Locate and identify every blood parasite.
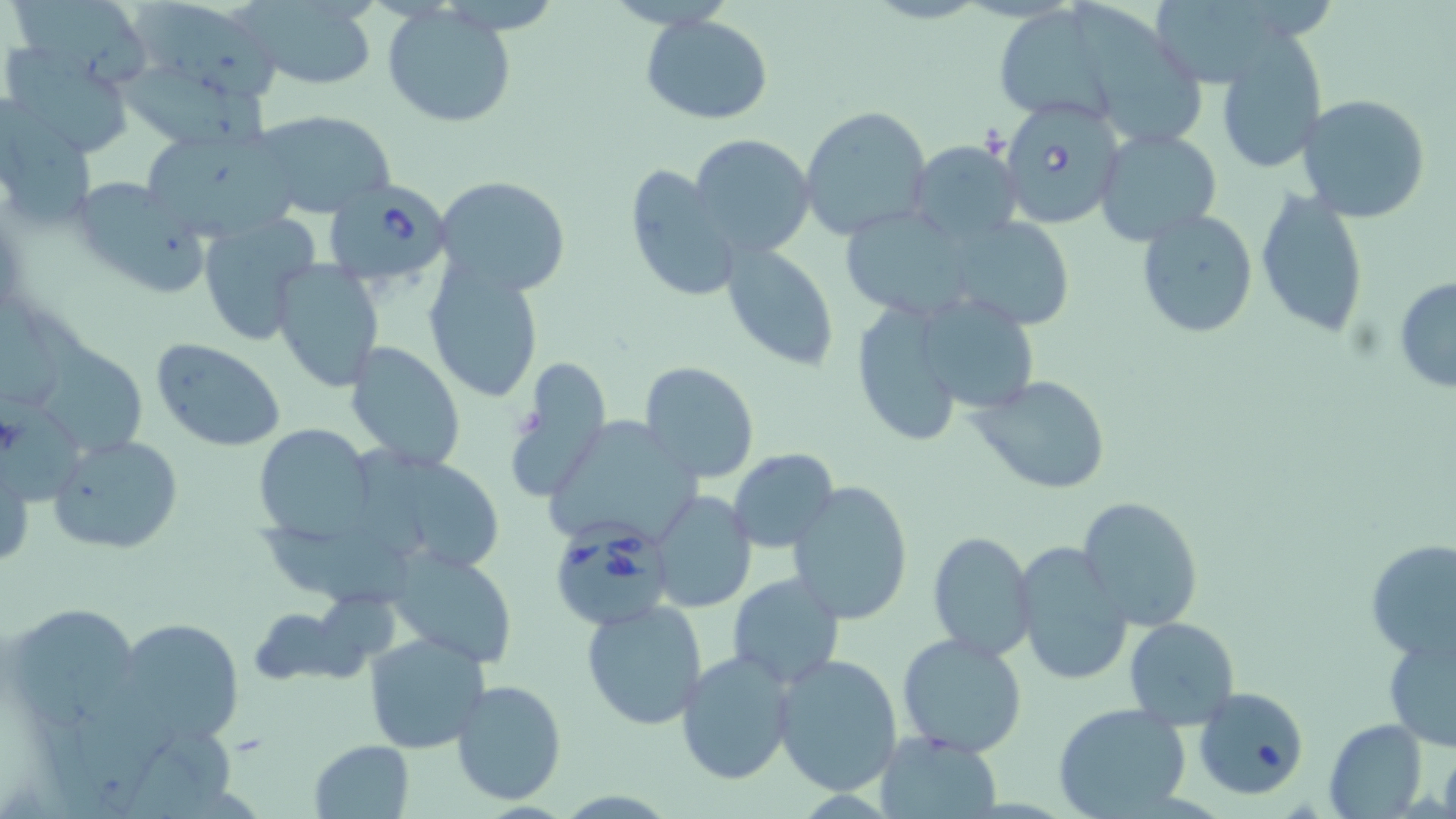
Approximate bounding boxes as [x1, y1, x2, y2] in pixels.
Babesia divergens-infected red blood cells: [995, 98, 1126, 229], [326, 177, 455, 289], [549, 515, 677, 630], [1193, 686, 1310, 801].
No Plasmodium falciparum, Plasmodium ovale, Plasmodium malariae, Plasmodium vivax, or Trypanosoma brucei observed.

slide_level_diagnosis: Babesia divergens
magnification: 1000x
field_of_view: single
preparation: thin blood smear
stain: May-Grünwald-Giemsa
modality: optical microscopy
image_size: 1456×819 pixels
uninfected_red_blood_cell_locations: 'approximate bounding boxes as [x1, y1, x2, y2] in pixels: [12, 0, 152, 93], [1075, 0, 1211, 151], [237, 3, 378, 89], [121, 4, 292, 98], [382, 7, 517, 127], [995, 8, 1112, 122], [641, 15, 773, 124], [1212, 33, 1327, 174], [4, 45, 139, 159], [106, 60, 270, 145], [1298, 93, 1431, 223], [0, 94, 92, 231], [799, 107, 933, 243], [253, 109, 397, 220], [1094, 128, 1222, 247], [139, 131, 311, 237], [689, 133, 816, 258], [906, 140, 1024, 247], [624, 164, 741, 304], [433, 174, 571, 298], [71, 181, 208, 300], [1254, 187, 1370, 338], [849, 207, 968, 317], [1135, 208, 1258, 338], [200, 212, 323, 342], [943, 215, 1081, 332], [719, 241, 840, 372], [273, 259, 385, 393], [425, 261, 544, 405], [1393, 274, 1456, 395], [915, 296, 1041, 414], [857, 302, 957, 447], [37, 320, 148, 452], [151, 338, 287, 452], [345, 341, 467, 471], [500, 359, 612, 507], [639, 362, 760, 483], [971, 375, 1112, 494], [541, 407, 704, 541], [254, 425, 376, 541], [48, 434, 183, 553], [351, 448, 504, 575], [729, 448, 838, 552], [787, 480, 914, 627], [650, 491, 755, 613], [1077, 495, 1204, 631], [255, 523, 416, 607], [926, 530, 1036, 663], [1364, 539, 1455, 662], [1013, 541, 1136, 689], [388, 547, 519, 670], [727, 574, 844, 688], [581, 600, 709, 731], [11, 603, 136, 728], [111, 617, 246, 747], [1123, 617, 1240, 730], [1384, 629, 1456, 750], [362, 631, 491, 753], [897, 633, 1028, 757], [675, 650, 798, 784], [772, 654, 905, 798], [450, 679, 566, 806], [1051, 702, 1191, 818], [1323, 719, 1428, 817], [873, 729, 1004, 817], [307, 740, 415, 819]'